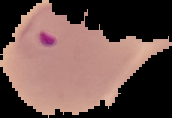

Image is 172×118 pixels. From a thin blood smear. Malaria status: parasitized. Segmented cell region on a black background.